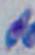
Micrograph. 1000x magnification. Toxoplasma gondii is shown.